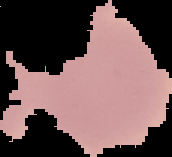

Summary:
  - Image size: 172×157 pixels
  - Image type: cell region segmented out of the field of view; surrounding area masked to black
  - Result: no Plasmodium parasites detected
  - Preparation: thin blood film